Identify the parasite.
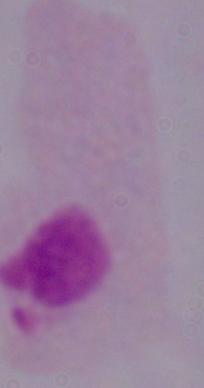
This is a trichomonad.

Photomicrograph. 1000x magnification.